Give the extent of all uninfected red blood cells.
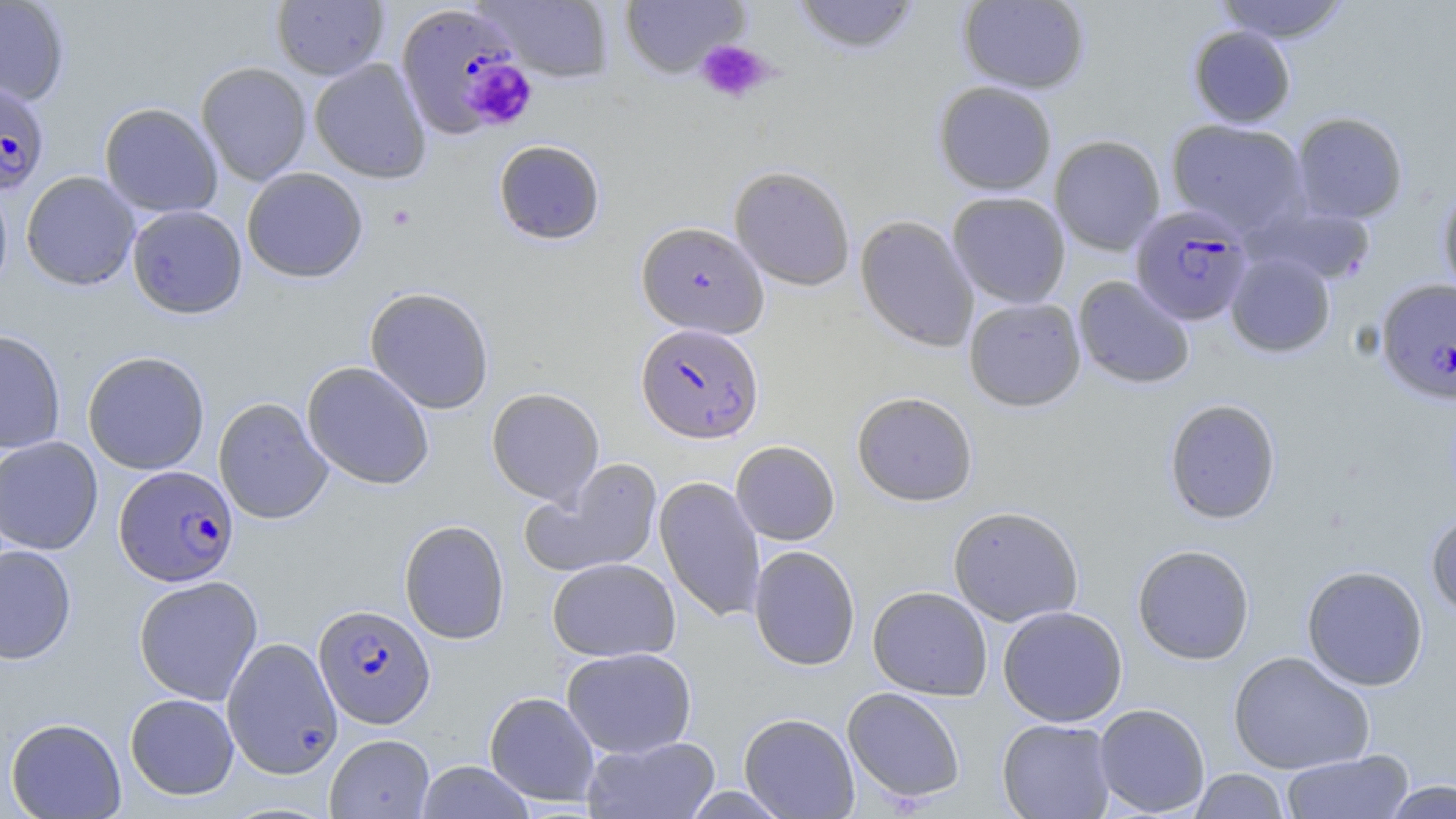

Approximate bounding boxes as [x1, y1, x2, y2] in pixels.
Uninfected red blood cells (subset): [0, 0, 70, 105], [477, 0, 615, 83], [619, 0, 750, 79], [791, 0, 921, 54], [1213, 0, 1351, 43], [271, 1, 389, 80], [958, 1, 1090, 94], [1188, 26, 1296, 127], [310, 58, 432, 183], [196, 61, 312, 186], [933, 81, 1057, 195], [99, 102, 223, 218], [1291, 111, 1408, 223], [1166, 119, 1311, 236], [1049, 135, 1165, 255], [493, 139, 606, 245], [729, 165, 855, 291], [242, 167, 368, 283], [21, 171, 140, 291], [0, 177, 13, 301], [1437, 182, 1456, 302], [947, 191, 1071, 307], [127, 204, 247, 318], [855, 215, 979, 352], [1225, 251, 1336, 358], [1073, 275, 1196, 389], [364, 286, 495, 414], [963, 297, 1086, 411], [0, 330, 66, 453], [82, 350, 210, 475], [301, 361, 435, 489], [486, 387, 604, 506], [852, 391, 978, 506], [214, 397, 333, 524], [1164, 398, 1282, 524], [0, 436, 103, 555], [731, 440, 840, 545], [522, 458, 663, 578], [654, 475, 765, 624], [948, 506, 1084, 626], [1426, 510, 1456, 617], [399, 519, 510, 644], [0, 544, 77, 664], [1132, 544, 1255, 665], [749, 545, 860, 671], [547, 557, 680, 662], [1301, 564, 1429, 691], [133, 575, 263, 705], [867, 586, 993, 700], [998, 605, 1128, 726], [222, 637, 343, 778], [561, 647, 697, 758], [1228, 650, 1375, 775], [842, 686, 966, 805], [485, 691, 600, 806], [125, 693, 239, 800], [1093, 703, 1210, 817], [739, 712, 860, 818], [6, 717, 126, 818], [997, 718, 1117, 819], [325, 734, 434, 818], [582, 735, 721, 819], [1281, 750, 1413, 819], [416, 761, 535, 818], [1189, 768, 1290, 818], [1382, 779, 1455, 818].

Platelet locations: [697, 40, 774, 104], [464, 59, 537, 130]. Plasmodium falciparum-infected red blood cell locations (subset): [395, 4, 527, 139], [0, 80, 50, 196], [1130, 206, 1253, 326], [1376, 277, 1456, 404], [635, 322, 764, 443], [114, 464, 239, 587], [314, 604, 435, 728]. Slide-level diagnosis: Plasmodium falciparum. 1000x magnification. Image is 1456×819 pixels. Single field of view. May-Grünwald-Giemsa stain. Thin blood smear. Light microscopy.